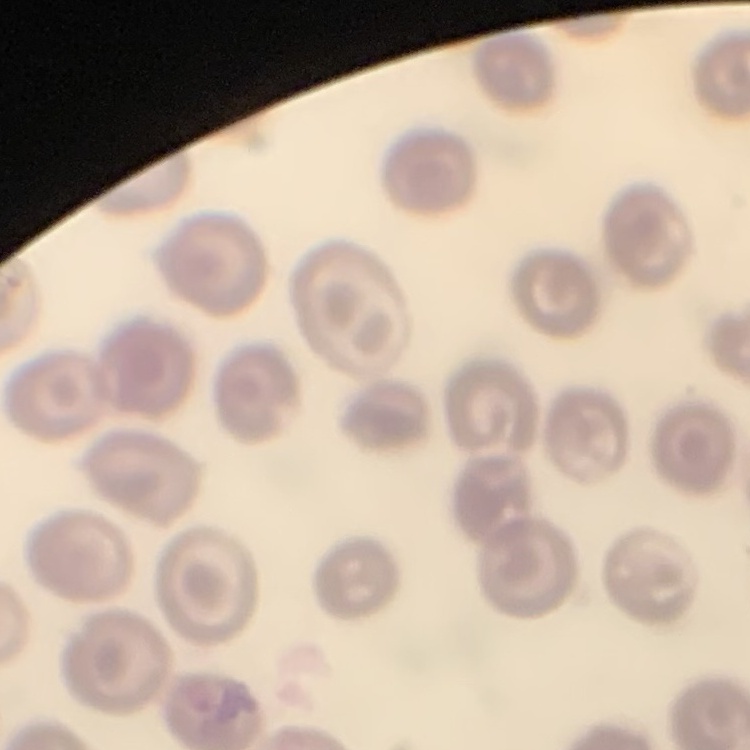

The erythrocytes exhibit no rouleaux formation. Thin blood smear. One tile cut from a larger photomicrograph. Stained with either Field's or Giemsa.